Name the blood parasite species.
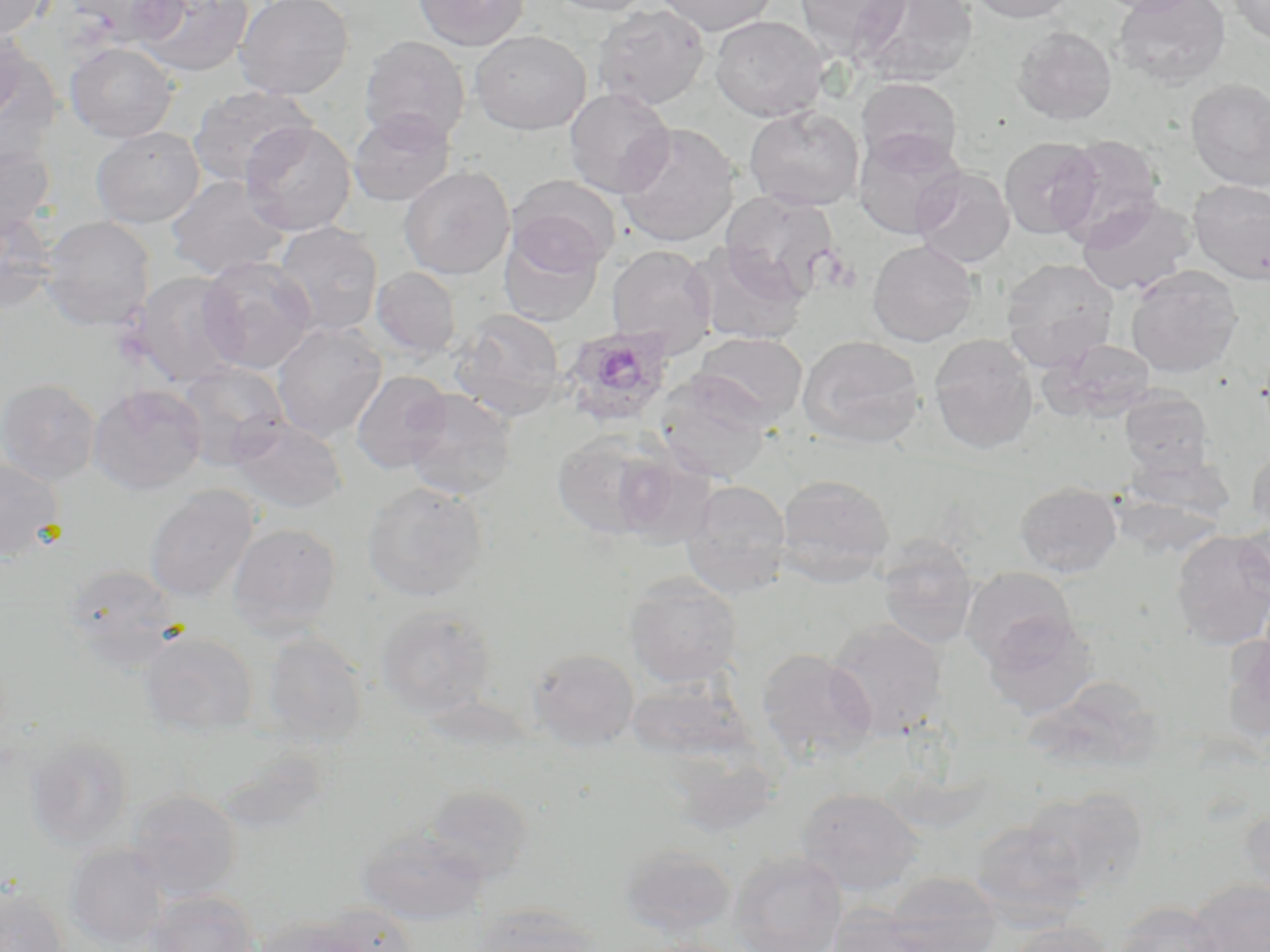

Plasmodium ovale.

platelet locations = approximate bounding boxes as [x1, y1, x2, y2] in pixels: [819, 249, 860, 295]
field of view = one of a larger specimen
stain = May-Grünwald-Giemsa
Plasmodium ovale-infected red blood cell locations = approximate bounding boxes as [x1, y1, x2, y2] in pixels: [559, 325, 676, 428]
image size = 1270×952 pixels
modality = light microscopy
magnification = 1000x
preparation = thin blood smear
uninfected red blood cell locations = approximate bounding boxes as [x1, y1, x2, y2] in pixels: [0, 0, 50, 40], [0, 0, 46, 82], [68, 0, 186, 46], [132, 0, 254, 78], [234, 0, 354, 100], [413, 0, 529, 51], [546, 0, 658, 16], [656, 0, 777, 36], [794, 0, 910, 58], [854, 0, 978, 86], [967, 0, 1076, 23], [1092, 0, 1201, 15], [1113, 0, 1231, 89], [1228, 0, 1270, 46], [592, 3, 711, 110], [710, 15, 828, 122], [0, 25, 29, 122], [1012, 26, 1117, 125], [471, 30, 590, 135], [359, 35, 471, 147], [65, 42, 178, 142], [855, 76, 963, 171], [1186, 78, 1270, 191], [189, 85, 315, 187], [564, 87, 675, 198], [744, 105, 865, 211], [348, 108, 456, 207], [241, 121, 357, 236], [614, 123, 740, 248], [91, 126, 205, 228], [853, 130, 965, 239], [1054, 135, 1165, 245], [998, 136, 1102, 240], [0, 139, 55, 240], [399, 165, 515, 279], [911, 167, 1015, 269], [165, 175, 291, 279], [507, 175, 621, 272], [1188, 180, 1270, 284], [719, 191, 840, 300], [1076, 196, 1196, 296], [0, 209, 58, 313], [40, 216, 156, 330], [272, 221, 383, 336], [499, 225, 604, 327], [867, 240, 978, 347], [688, 242, 809, 345], [606, 245, 717, 356], [198, 256, 318, 374], [1000, 257, 1119, 370], [1125, 265, 1243, 378], [371, 267, 462, 359], [128, 271, 246, 388], [451, 309, 567, 421], [272, 322, 387, 441], [692, 332, 808, 427], [929, 334, 1039, 455], [797, 335, 926, 447], [1041, 339, 1157, 421], [174, 361, 290, 469], [351, 370, 452, 473], [653, 374, 773, 484], [0, 378, 101, 485], [88, 384, 207, 494], [402, 388, 517, 501], [1120, 390, 1213, 474], [229, 417, 346, 513], [551, 430, 671, 540], [1246, 445, 1270, 536], [1123, 446, 1234, 522], [611, 450, 717, 549], [0, 456, 65, 561], [775, 474, 895, 587], [681, 479, 792, 598], [362, 481, 488, 602], [1015, 482, 1121, 578], [144, 485, 259, 603], [1236, 521, 1270, 602], [227, 522, 342, 635], [1170, 530, 1270, 650], [876, 538, 980, 649], [62, 563, 183, 666], [961, 566, 1077, 668], [623, 573, 742, 689], [375, 607, 497, 719], [983, 613, 1098, 719], [825, 617, 948, 741], [138, 631, 258, 737], [262, 632, 368, 746], [1221, 634, 1270, 743], [527, 647, 640, 750], [756, 648, 877, 765], [625, 677, 755, 762], [25, 735, 135, 850], [664, 746, 781, 838], [423, 784, 535, 883], [795, 786, 925, 896], [1023, 788, 1148, 898], [124, 789, 242, 899], [1238, 803, 1270, 905], [969, 820, 1092, 925], [356, 827, 489, 925], [65, 843, 170, 948], [618, 843, 737, 940], [729, 849, 849, 952], [882, 872, 1003, 952], [1188, 878, 1270, 952], [0, 883, 68, 952], [144, 890, 260, 952], [1112, 901, 1227, 952], [470, 903, 601, 952], [312, 904, 420, 952], [824, 907, 947, 952], [252, 917, 367, 952], [1005, 921, 1114, 952], [633, 937, 751, 952]